Describe the morphology of the erythrocytes.
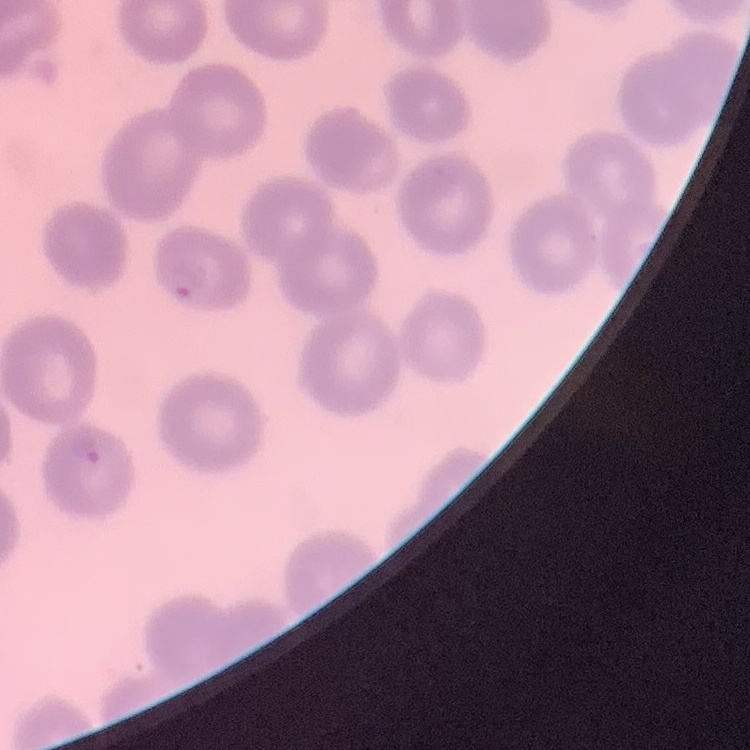

They show no rouleaux formation.

image type = square crop of a larger photomicrograph
stain = Field's or Giemsa
preparation = thin blood film